Comment on the morphology of the red blood cells.
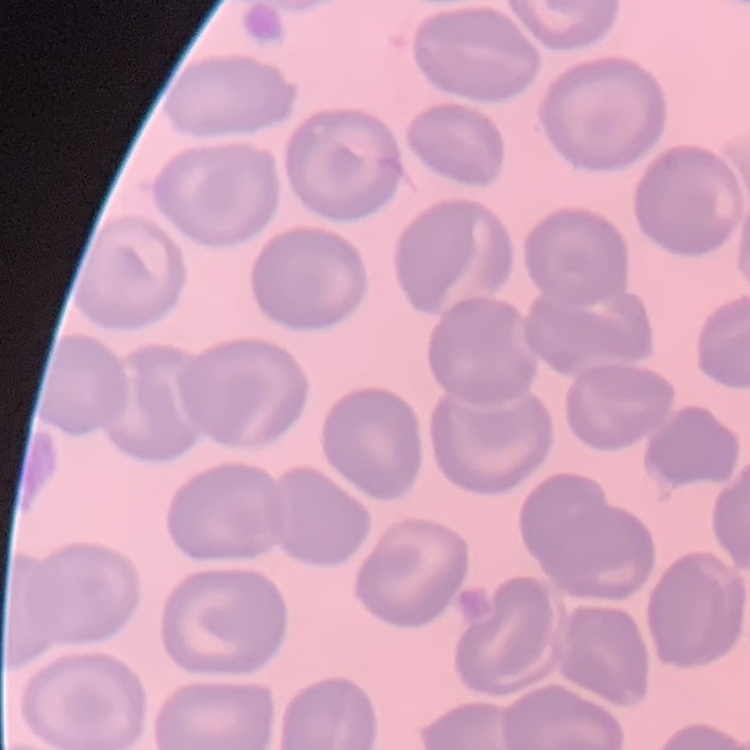

No rouleaux formation.

Summary:
  - Stain: Field's or Giemsa
  - Preparation: thin peripheral smear
  - Image type: one tile cut from a larger photomicrograph